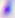
Summary:
  - Identification: Toxoplasma gondii
  - Modality: micrograph
  - Magnification: 400x